Describe the morphology of the red blood cells.
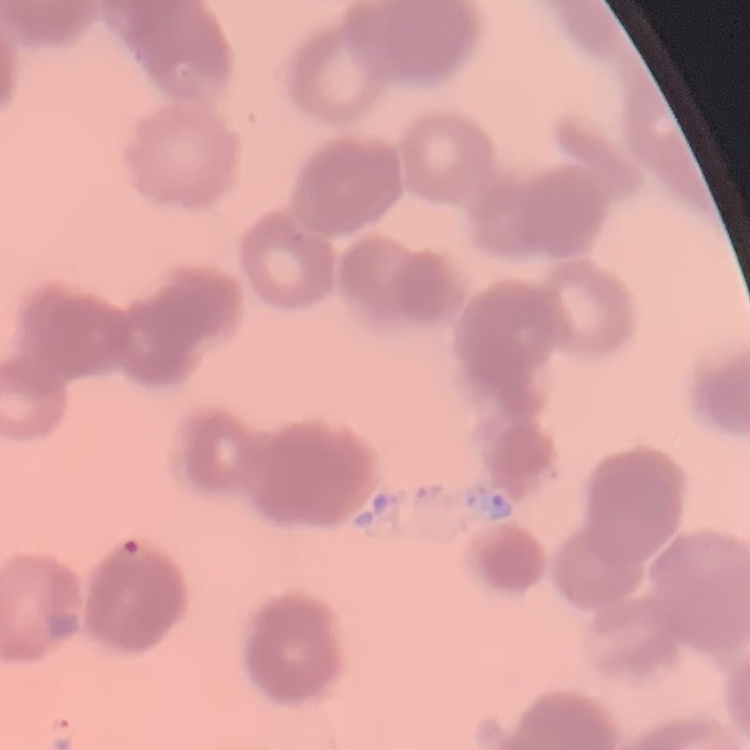

They show rouleaux formation.

image type = one tile cut from a larger photomicrograph
preparation = thin blood film
stain = Field's or Giemsa